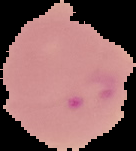

{
  "image_type": "segmented cell region on a black background",
  "preparation": "thin blood smear",
  "image_size": "136×151 pixels",
  "result": "malaria parasites identified"
}